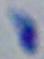
Summary:
  - Identification: Toxoplasma gondii
  - Magnification: 1000x
  - Modality: photomicrograph